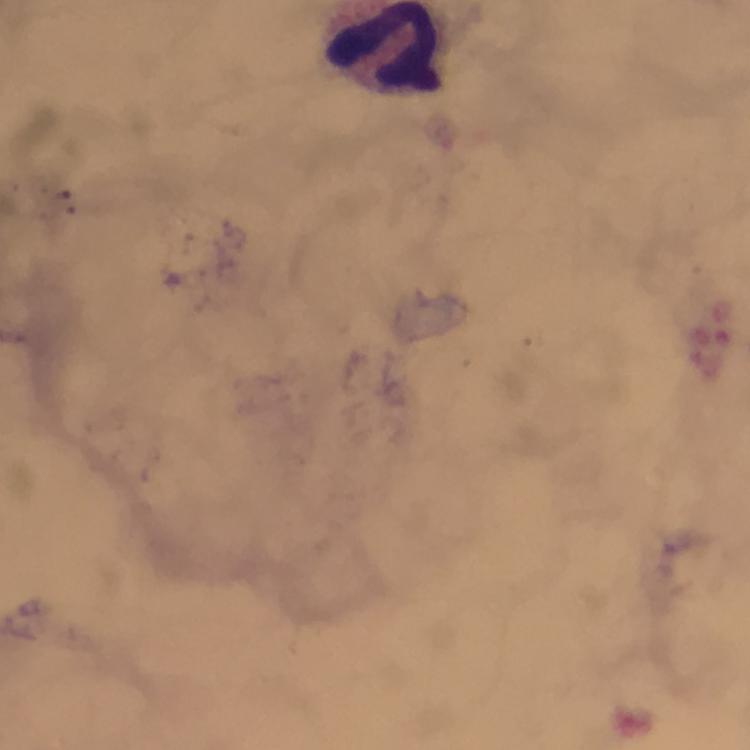

preparation = thick blood smear
cropped from = a single field of view
malaria parasites = none seen
leukocyte locations = approximate centers as [x, y] in pixels: [382, 49]
image size = 750×750 pixels
magnification = 100x
immersion oil = applied
capture = smartphone camera through the microscope
context = from a diagnostic examination for malaria
stain = Giemsa